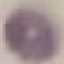

malaria status = uninfected
image type = automatically extracted cell patch, resized to 64 × 64 pixels
capture = smartphone through the microscope eyepiece
preparation = thin blood film
stain = Giemsa